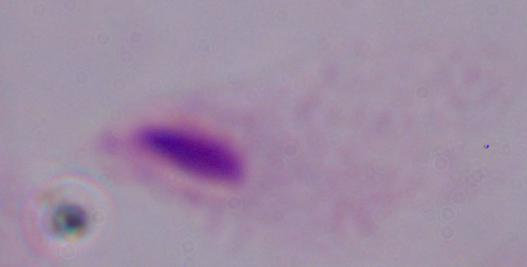 Captured at 1000x magnification. Photomicrograph. A trichomonad is seen.